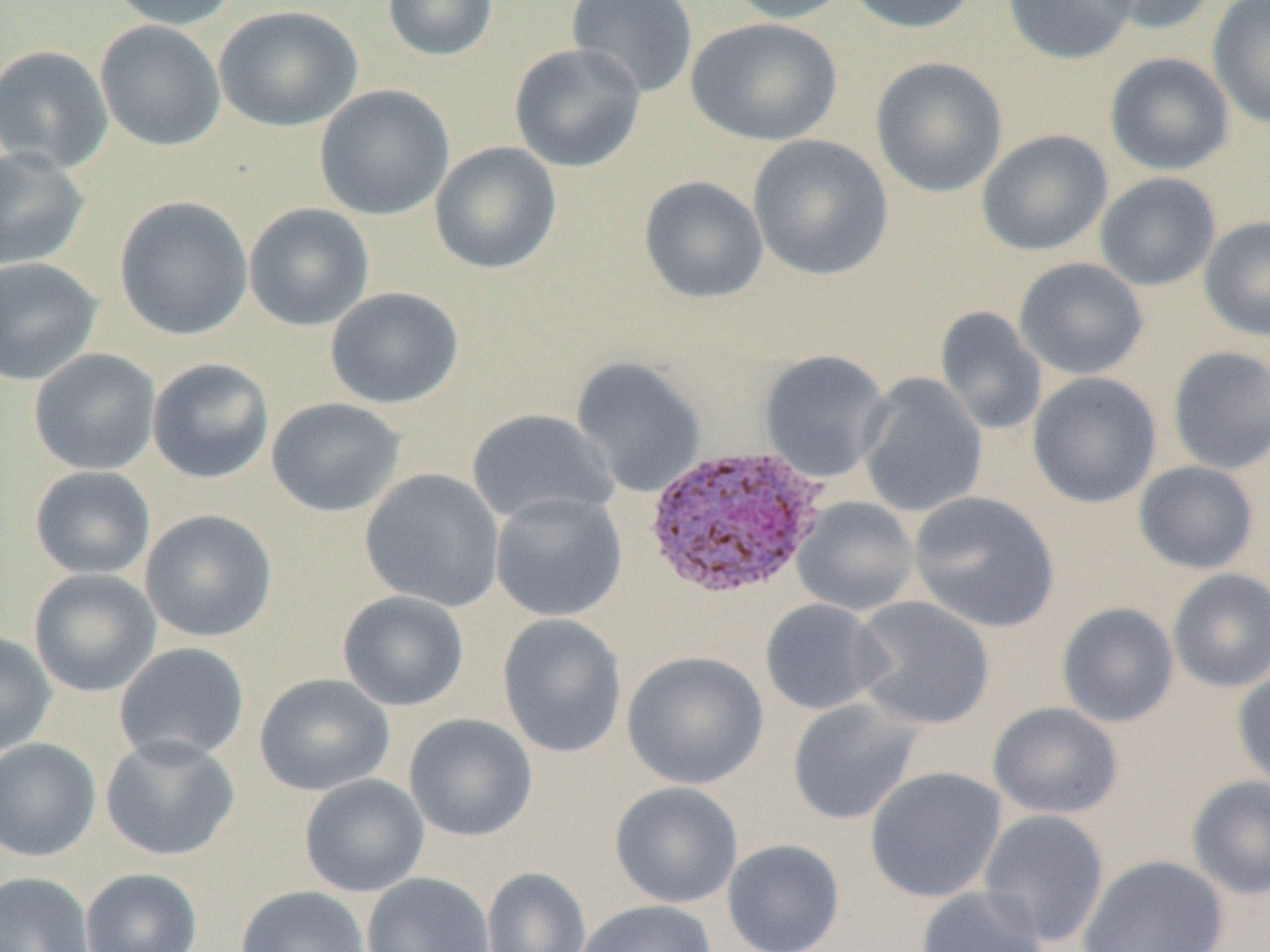

{
  "slide_level_diagnosis": "Plasmodium ovale",
  "uninfected_red_blood_cell_locations": "approximate bounding boxes as named x1/y1/x2/y2 corners in pixels: (x1=107, y1=0, x2=241, y2=30), (x1=382, y1=0, x2=499, y2=62), (x1=567, y1=0, x2=699, y2=99), (x1=722, y1=0, x2=851, y2=24), (x1=842, y1=0, x2=982, y2=34), (x1=1002, y1=0, x2=1138, y2=64), (x1=1087, y1=0, x2=1219, y2=35), (x1=1207, y1=0, x2=1270, y2=129), (x1=214, y1=5, x2=363, y2=132), (x1=686, y1=17, x2=843, y2=146), (x1=95, y1=20, x2=226, y2=151), (x1=509, y1=42, x2=646, y2=173), (x1=0, y1=45, x2=114, y2=173), (x1=1104, y1=51, x2=1234, y2=175), (x1=870, y1=56, x2=1009, y2=198), (x1=314, y1=84, x2=455, y2=221), (x1=977, y1=129, x2=1113, y2=256), (x1=747, y1=134, x2=894, y2=282), (x1=429, y1=141, x2=562, y2=275), (x1=0, y1=147, x2=90, y2=271), (x1=1094, y1=172, x2=1221, y2=291), (x1=638, y1=176, x2=769, y2=304), (x1=113, y1=195, x2=254, y2=341), (x1=244, y1=203, x2=375, y2=331), (x1=1199, y1=215, x2=1270, y2=342), (x1=0, y1=257, x2=103, y2=385), (x1=1013, y1=257, x2=1149, y2=380), (x1=324, y1=287, x2=465, y2=409), (x1=934, y1=306, x2=1047, y2=436), (x1=1167, y1=345, x2=1270, y2=475), (x1=28, y1=348, x2=162, y2=476), (x1=758, y1=350, x2=892, y2=483), (x1=570, y1=356, x2=707, y2=498), (x1=147, y1=357, x2=275, y2=484), (x1=1027, y1=371, x2=1162, y2=509), (x1=857, y1=373, x2=988, y2=518), (x1=266, y1=397, x2=407, y2=518), (x1=466, y1=408, x2=619, y2=527), (x1=1134, y1=460, x2=1259, y2=574), (x1=29, y1=466, x2=156, y2=580), (x1=360, y1=468, x2=506, y2=612), (x1=908, y1=490, x2=1060, y2=633), (x1=489, y1=491, x2=628, y2=622), (x1=791, y1=496, x2=919, y2=617), (x1=140, y1=509, x2=279, y2=643), (x1=28, y1=568, x2=162, y2=697), (x1=1167, y1=568, x2=1270, y2=693), (x1=337, y1=590, x2=470, y2=712), (x1=850, y1=596, x2=994, y2=730), (x1=760, y1=598, x2=891, y2=716), (x1=1057, y1=602, x2=1179, y2=728), (x1=497, y1=613, x2=627, y2=758), (x1=0, y1=631, x2=57, y2=757), (x1=113, y1=642, x2=250, y2=765), (x1=622, y1=650, x2=769, y2=790), (x1=1233, y1=666, x2=1270, y2=793), (x1=253, y1=673, x2=395, y2=796), (x1=787, y1=698, x2=923, y2=826), (x1=988, y1=702, x2=1123, y2=819), (x1=404, y1=713, x2=538, y2=842), (x1=100, y1=734, x2=240, y2=861), (x1=0, y1=738, x2=102, y2=862), (x1=864, y1=766, x2=1007, y2=903), (x1=299, y1=773, x2=429, y2=897), (x1=1186, y1=775, x2=1270, y2=900), (x1=609, y1=781, x2=743, y2=909), (x1=978, y1=808, x2=1110, y2=948), (x1=722, y1=838, x2=845, y2=952), (x1=1077, y1=854, x2=1229, y2=951), (x1=481, y1=866, x2=592, y2=952), (x1=80, y1=867, x2=203, y2=952), (x1=0, y1=871, x2=95, y2=952), (x1=361, y1=871, x2=495, y2=952), (x1=916, y1=884, x2=1048, y2=952), (x1=235, y1=885, x2=370, y2=952), (x1=574, y1=900, x2=717, y2=952)",
  "preparation": "thin blood smear",
  "field_of_view": "single",
  "plasmodium_ovale_infected_red_blood_cell_locations": "approximate bounding boxes as named x1/y1/x2/y2 corners in pixels: (x1=642, y1=444, x2=827, y2=600)",
  "modality": "light microscopy",
  "magnification": "1000x",
  "image_size": "1270×952 pixels"
}